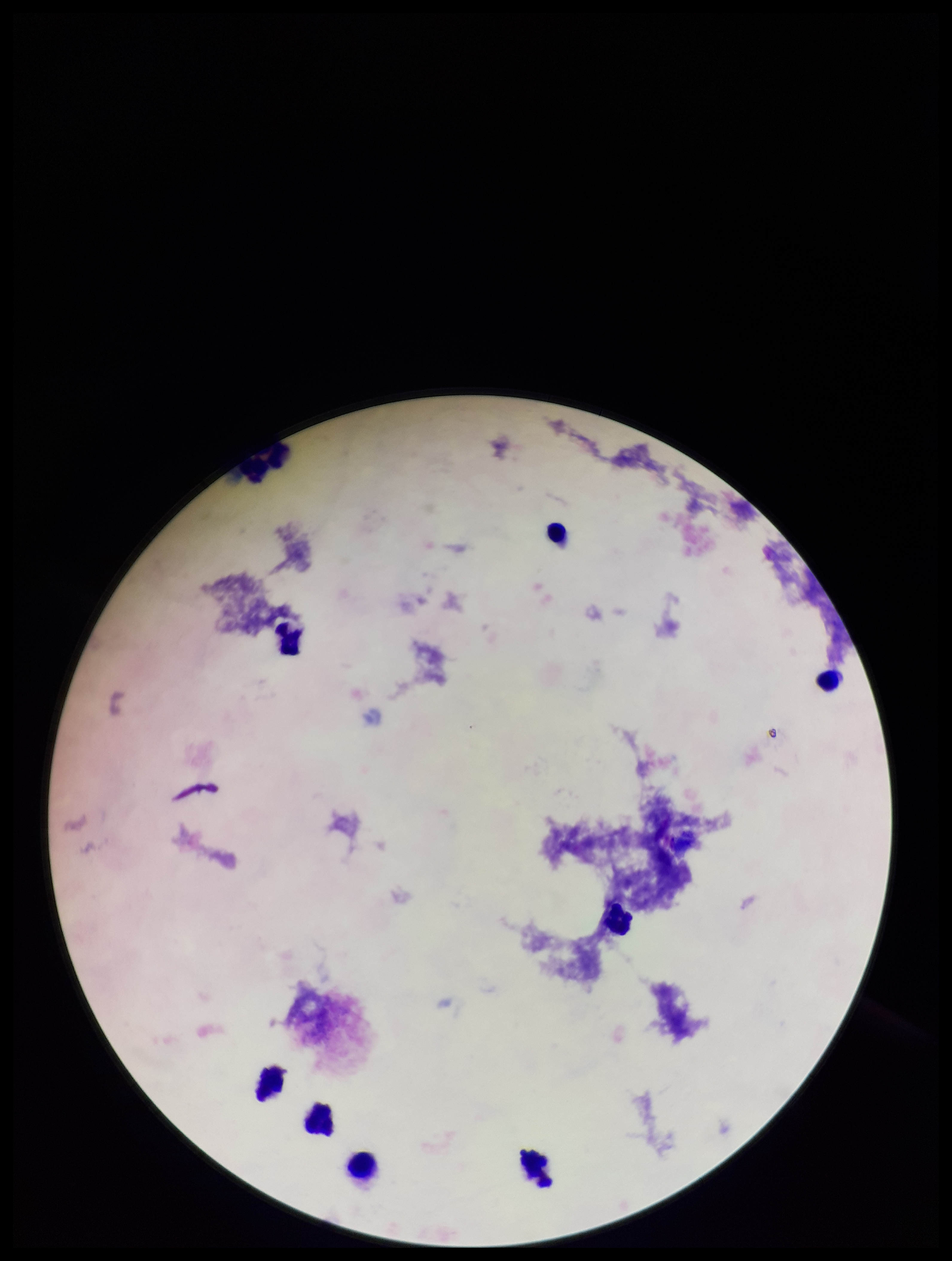

leukocyte_count: 8
capture: smartphone photograph through the microscope eyepiece
plasmodium_parasites: none identified
image_size: 952×1261 pixels
stain: Giemsa
parasite_count: 0
preparation: thick
patient_malaria_status: negative
field_of_view: one from this slide